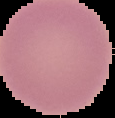
{
  "image_size": "115×118 pixels",
  "result": "negative for malaria parasites",
  "image_type": "segmented cell region on a black background",
  "preparation": "thin blood smear"
}